Outline each blood parasite and name the species.
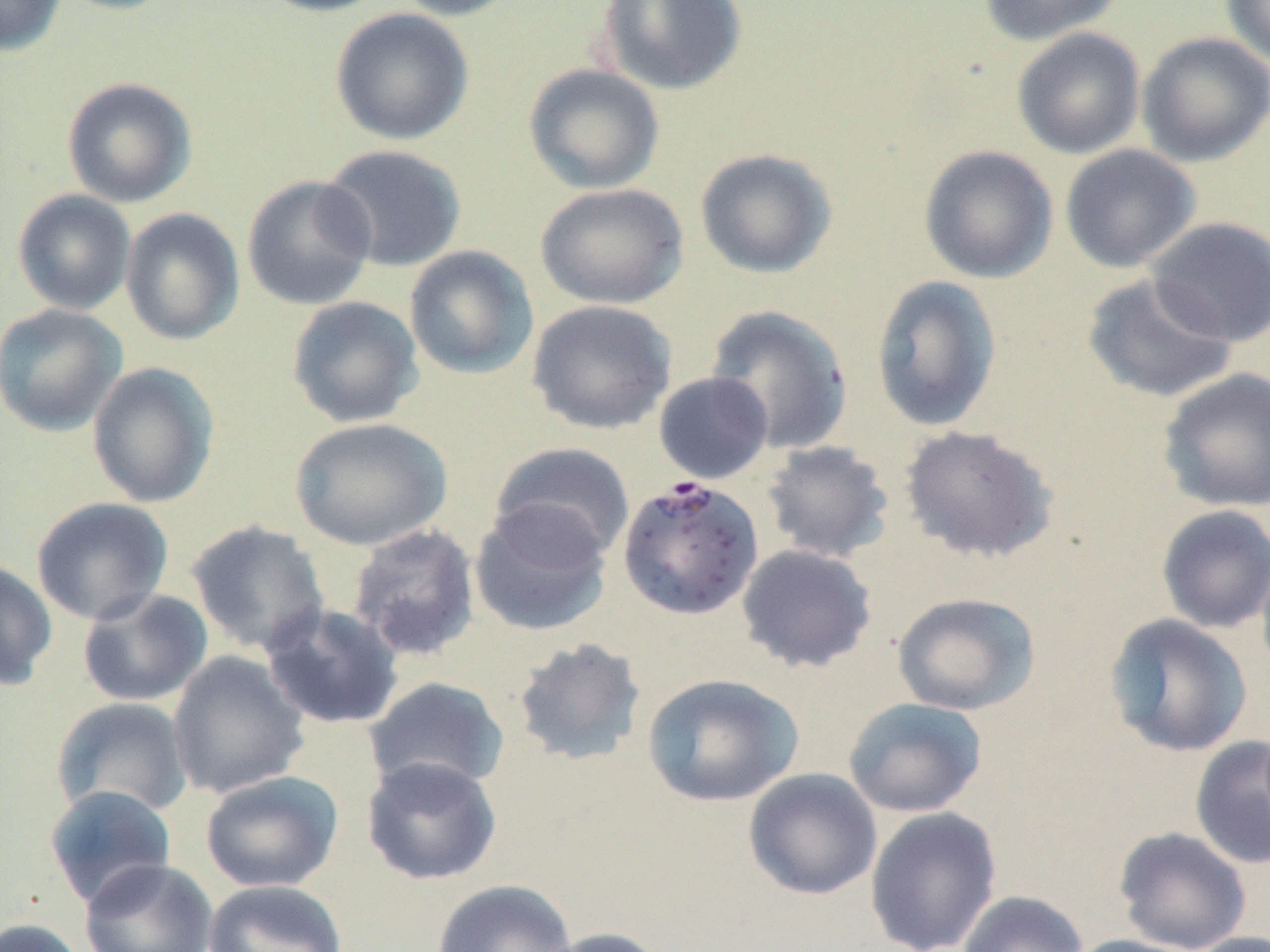
Approximate bounding boxes as (x1, y1, x2, y2) in pixels.
Plasmodium falciparum-infected red blood cells: (622, 471, 768, 618).
No Plasmodium ovale, Plasmodium malariae, Plasmodium vivax, Babesia divergens, or Trypanosoma brucei observed.

Summary:
  - Uninfected red blood cell locations: (0, 0, 67, 56), (52, 0, 182, 16), (252, 0, 394, 17), (389, 0, 525, 21), (596, 0, 748, 95), (978, 0, 1123, 45), (1218, 0, 1270, 66), (330, 8, 474, 145), (1011, 27, 1146, 159), (1136, 31, 1270, 167), (523, 62, 665, 195), (61, 77, 198, 209), (319, 144, 467, 272), (1060, 144, 1202, 273), (918, 145, 1058, 284), (694, 148, 838, 279), (241, 174, 377, 310), (534, 182, 688, 310), (12, 189, 137, 315), (120, 207, 245, 346), (1145, 216, 1270, 347), (403, 245, 539, 380), (1081, 273, 1238, 404), (870, 275, 1003, 432), (286, 295, 424, 429), (526, 299, 676, 436), (0, 302, 129, 437), (705, 304, 854, 455), (86, 361, 220, 509), (1157, 367, 1270, 514), (653, 371, 774, 484), (289, 417, 453, 551), (898, 425, 1059, 564), (761, 440, 895, 564), (490, 441, 636, 564), (30, 496, 174, 626), (469, 499, 612, 637), (1156, 504, 1270, 633), (186, 520, 331, 656), (347, 523, 481, 662), (736, 544, 877, 673), (0, 559, 58, 690), (77, 588, 213, 708), (891, 591, 1041, 715), (259, 603, 405, 730), (1104, 613, 1253, 758), (511, 637, 647, 767), (166, 650, 310, 800), (641, 673, 804, 808), (364, 676, 511, 794), (51, 697, 194, 819), (843, 697, 988, 817), (1189, 735, 1270, 871), (361, 755, 502, 885), (743, 768, 883, 901), (200, 770, 345, 893), (44, 784, 177, 910), (864, 805, 1002, 952), (1113, 827, 1252, 952), (79, 858, 218, 952), (203, 879, 349, 952), (432, 879, 576, 952), (957, 890, 1088, 952), (0, 917, 90, 952), (540, 926, 670, 952), (1185, 932, 1270, 952), (1065, 934, 1205, 952)
  - Slide-level diagnosis: Plasmodium falciparum
  - Preparation: thin blood film
  - Stain: May-Grünwald-Giemsa
  - Modality: optical microscopy
  - Magnification: 1000x
  - Field of view: single
  - Image size: 1270×952 pixels